State which parasite is depicted.
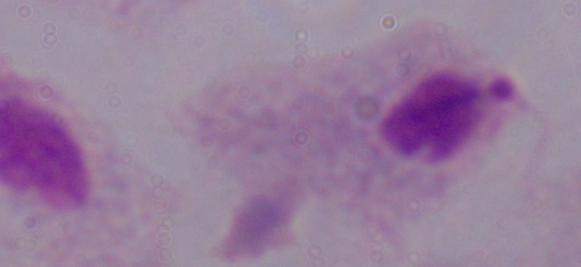

A trichomonad.

magnification = 1000x
modality = micrograph